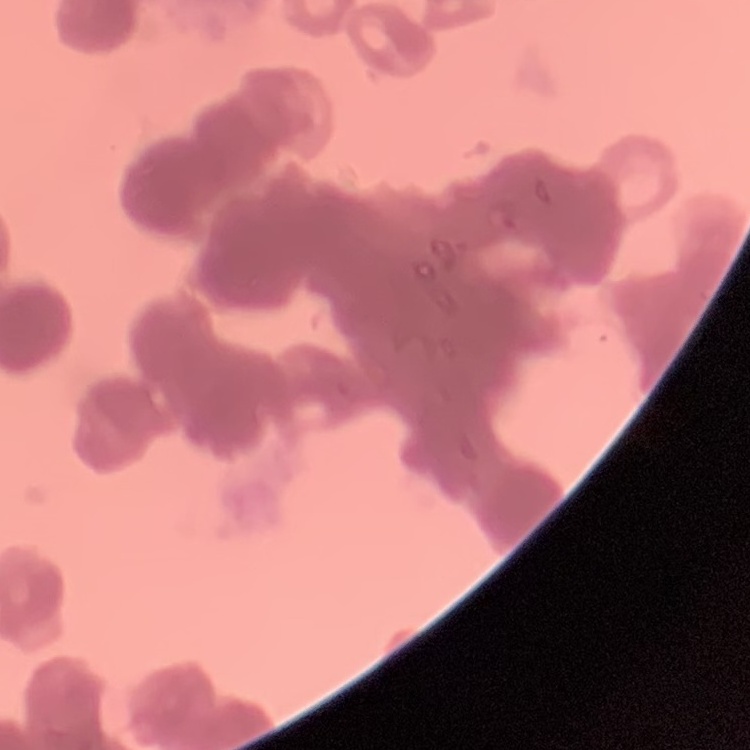

Summary:
  - Red blood cell morphology: rouleaux formation
  - Stain: Field's or Giemsa
  - Image type: one tile cut from a larger photomicrograph
  - Preparation: thin blood smear